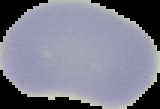

result = negative for malaria parasites
preparation = thin blood smear
image size = 160×109 pixels
image type = cell region segmented out of the field of view; surrounding area masked to black